Locate Plasmodium falciparum parasites and identify their life-cycle stages.
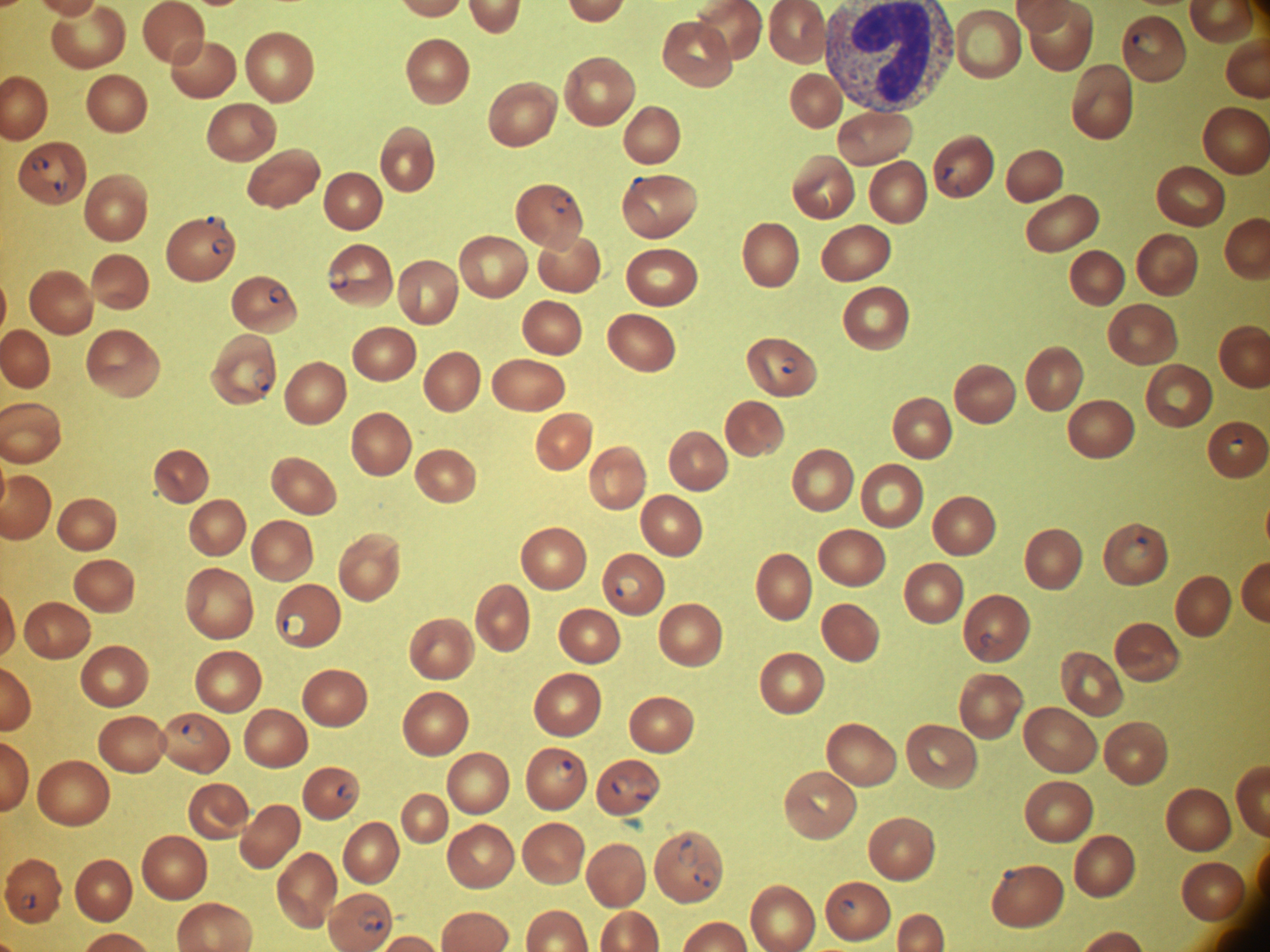

Approximate bounding boxes as (x1,y1)-(x2,y2) corner pairs in pixels, from the source annotation, which is not necessarily exhaustive.
Ring forms: (1132,31)-(1152,51), (30,155)-(51,172), (943,167)-(963,188), (53,178)-(68,197), (550,191)-(572,214), (206,215)-(226,231), (211,238)-(230,256), (326,268)-(349,289), (268,285)-(288,304), (779,356)-(798,375), (253,367)-(273,392), (1227,439)-(1246,457), (1128,536)-(1152,559), (616,575)-(643,597), (283,613)-(307,640), (182,720)-(207,746), (556,759)-(579,783), (611,776)-(630,795), (632,779)-(654,801), (337,783)-(355,802), (679,838)-(699,867), (694,861)-(718,888), (21,893)-(38,910), (838,900)-(857,915), (358,908)-(385,935).

Image is 1270×952 pixels. Leica DM2000 optical microscope with a built-in camera. Captured at 100x magnification. One field from this slide. Species: Plasmodium falciparum. Thin blood smear. Giemsa stain.